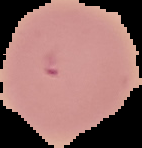 Result: no Plasmodium parasites detected. Image is 142×148 pixels. From a thin blood film. Cell region segmented out of the field of view; the surrounding area is masked to black.